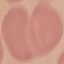

malaria status = uninfected
image type = cell patch, automatically extracted from a larger field of view and resized to 64 × 64 pixels
preparation = thin smear
capture = smartphone through the microscope eyepiece
stain = Giemsa